Give the extent of all uninfected red blood cells.
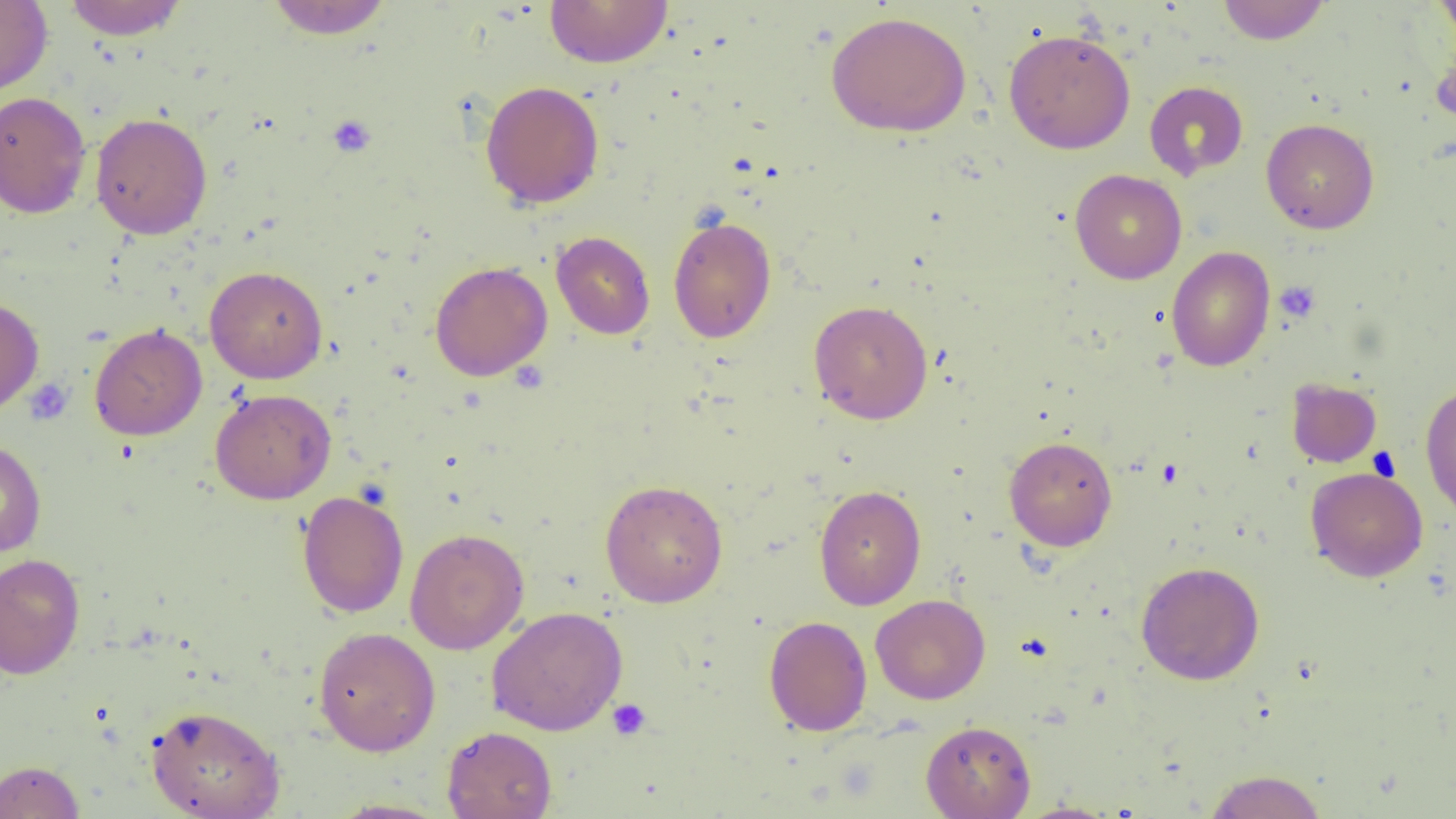
Approximate bounding boxes as [x1, y1, x2, y2] in pixels.
Uninfected red blood cells: [63, 0, 188, 40], [265, 0, 394, 39], [544, 0, 673, 68], [1217, 0, 1330, 44], [1434, 0, 1456, 48], [0, 1, 52, 96], [825, 11, 972, 137], [1004, 28, 1136, 154], [480, 80, 604, 209], [1144, 80, 1248, 180], [0, 91, 92, 218], [90, 112, 212, 239], [1261, 118, 1379, 234], [1070, 169, 1187, 284], [668, 216, 777, 343], [551, 231, 655, 339], [1166, 246, 1276, 372], [429, 260, 552, 381], [204, 265, 328, 384], [0, 296, 44, 415], [808, 299, 933, 424], [89, 323, 207, 440], [1286, 377, 1381, 467], [1420, 380, 1456, 521], [210, 388, 337, 505], [1004, 436, 1117, 551], [0, 437, 46, 557], [1305, 466, 1428, 582], [599, 479, 728, 607], [814, 485, 926, 610], [297, 490, 409, 618], [405, 528, 529, 655], [0, 552, 85, 680], [1136, 561, 1265, 685], [870, 594, 990, 704], [487, 606, 628, 735], [764, 615, 872, 735], [313, 626, 441, 756], [146, 704, 285, 819], [921, 720, 1035, 819], [441, 726, 557, 819], [0, 760, 84, 819], [1202, 769, 1328, 819], [327, 798, 451, 818], [1012, 801, 1122, 819].

Platelet locations: [326, 114, 377, 158], [1274, 280, 1321, 323], [23, 379, 73, 424], [607, 698, 652, 741]. Slide-level diagnosis: negative for blood parasites. Thin blood film. Captured at 1000x magnification. Optical microscopy. Image is 1456×819 pixels. Single field of view.